Comment on the morphology of the red blood cells.
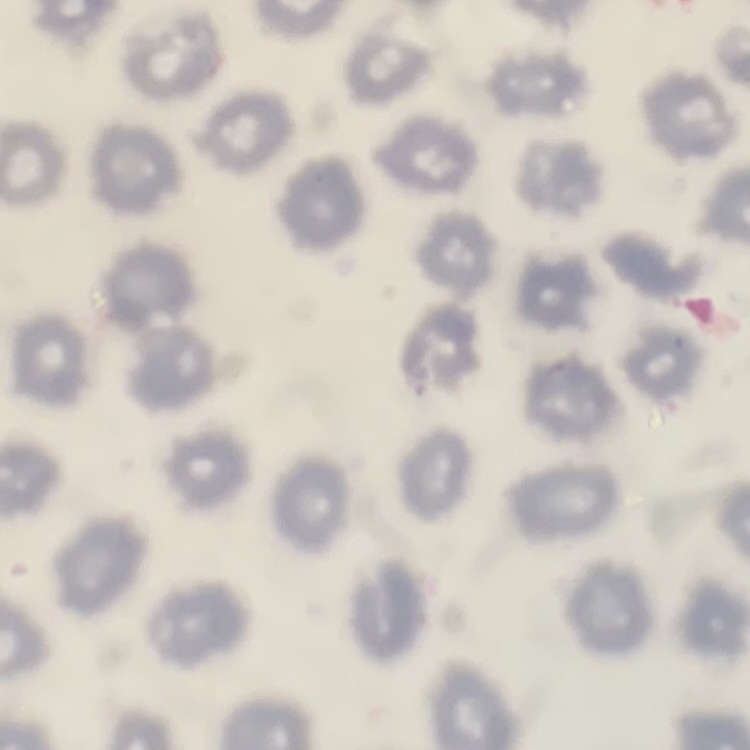
They show no rouleaux formation.

Summary:
  - Image type: one tile cut from a larger photomicrograph
  - Stain: Field's or Giemsa
  - Preparation: thin blood smear